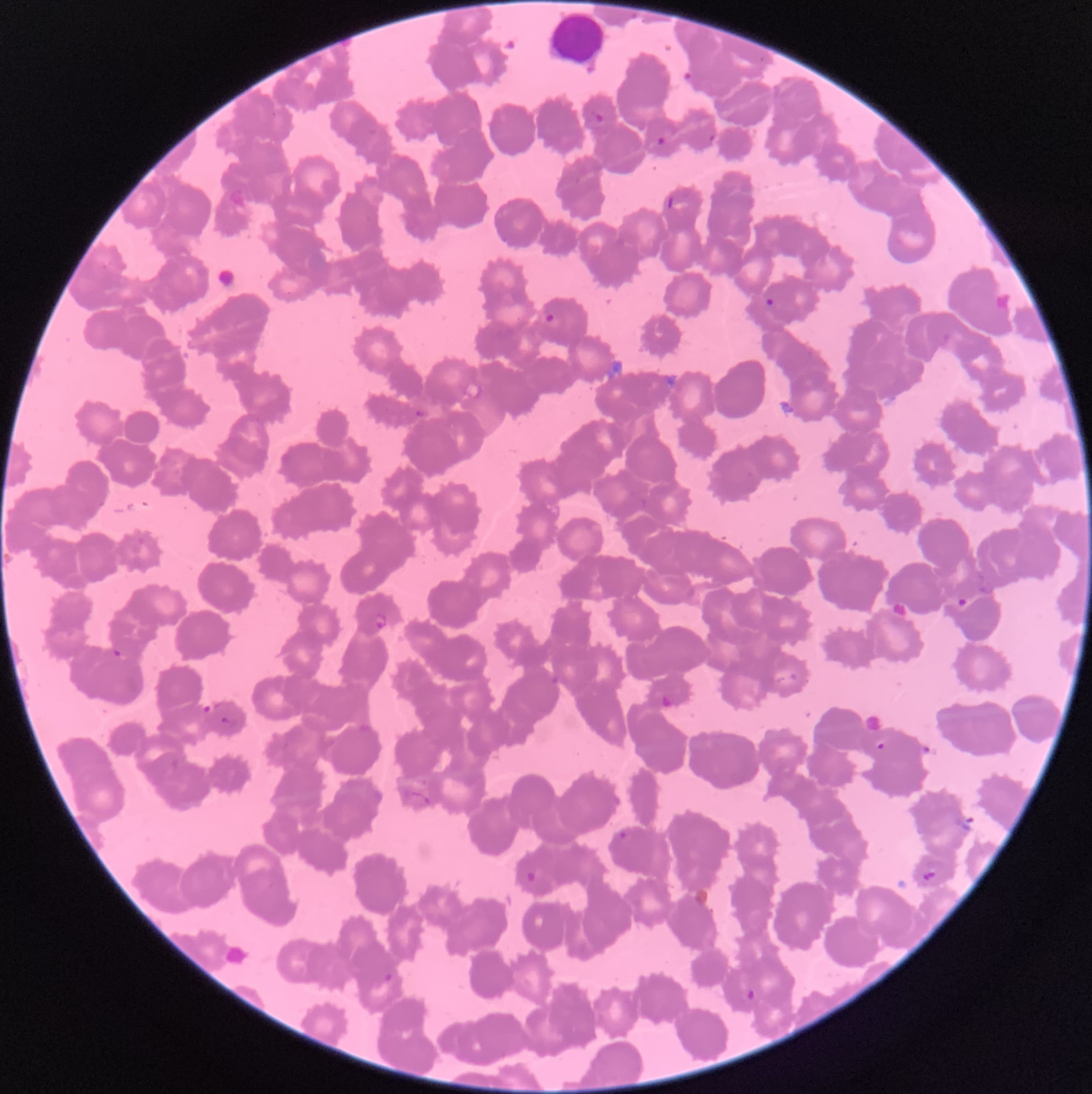
Approximate bounding boxes as (x1,y1)-(x2,y2) corner pairs in pixels. Plasmodium parasite locations: (587,111)-(603,126), (708,133)-(716,143), (657,136)-(667,146), (765,298)-(778,310), (545,313)-(556,324), (414,408)-(427,419), (955,597)-(971,608), (373,611)-(388,633), (111,648)-(128,663), (660,694)-(678,711), (199,703)-(213,716), (219,715)-(231,727), (873,739)-(887,750), (616,829)-(628,842), (922,869)-(938,880), (524,871)-(538,883), (383,972)-(394,983), (744,986)-(757,1004). Image is 1092×1094 pixels. Optical microscopy. The red blood cells show rouleaux formation. Thin blood film.